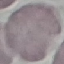
malaria status = uninfected
capture = smartphone through the microscope eyepiece
preparation = thin smear
stain = Giemsa
image type = automatically extracted cell patch, resized to 64 × 64 pixels